Assess this cell for malaria.
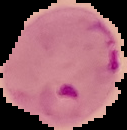

It is parasitized.

Summary:
  - Preparation: thin blood smear
  - Image type: cell region segmented out of the field of view; surrounding area masked to black
  - Image size: 127×130 pixels